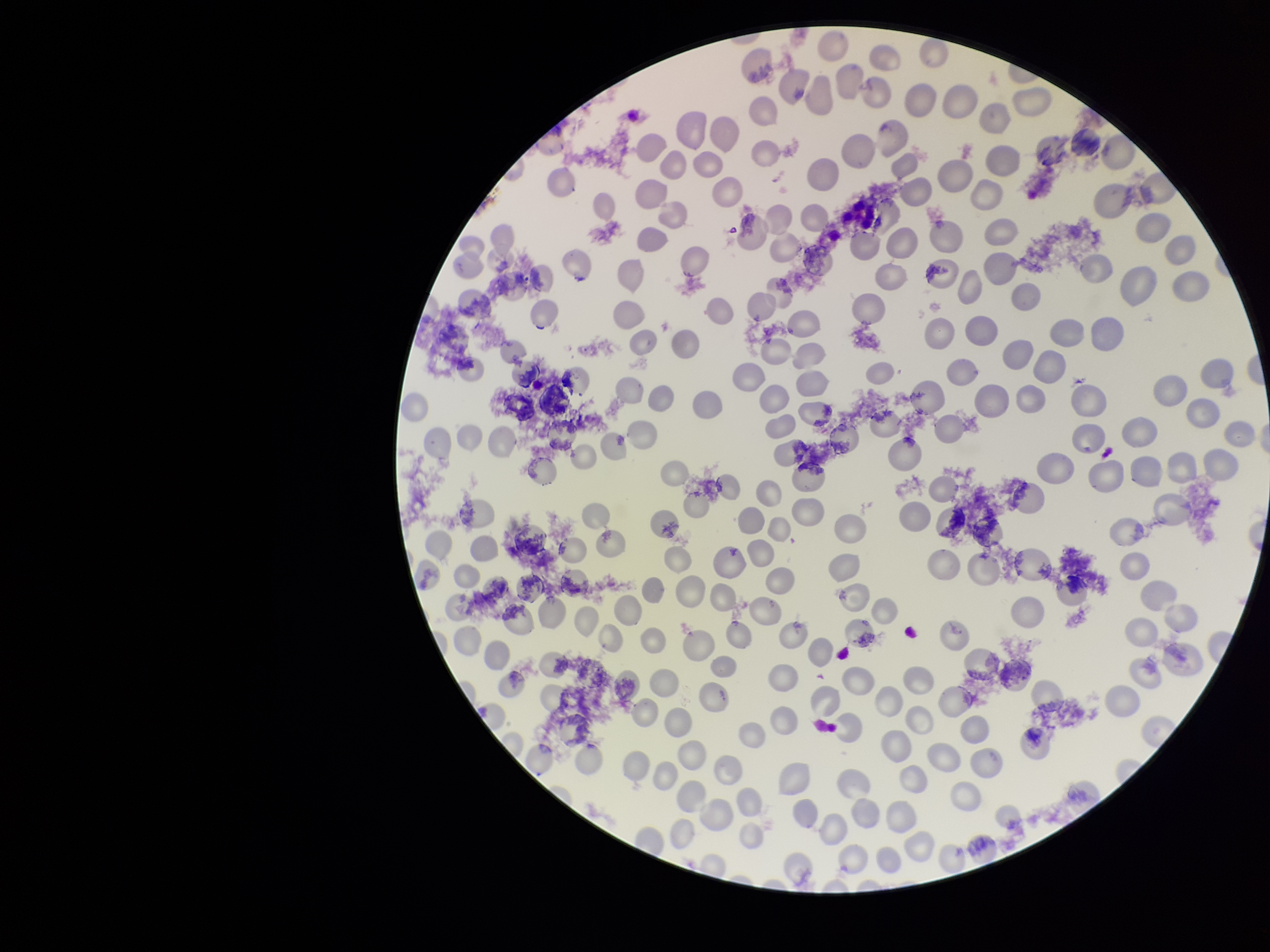

{
  "capture": "smartphone photograph through the microscope eyepiece",
  "parasitized_red_blood_cells": "none identified",
  "patient_malaria_status": "infected",
  "parasitized_red_blood_cell_count": 0,
  "preparation": "thin",
  "image_size": "1270×952 pixels",
  "red_blood_cell_count": 213,
  "stain": "Giemsa",
  "species_reported_for_this_patient": "Plasmodium vivax",
  "field_of_view": "one from this slide"
}